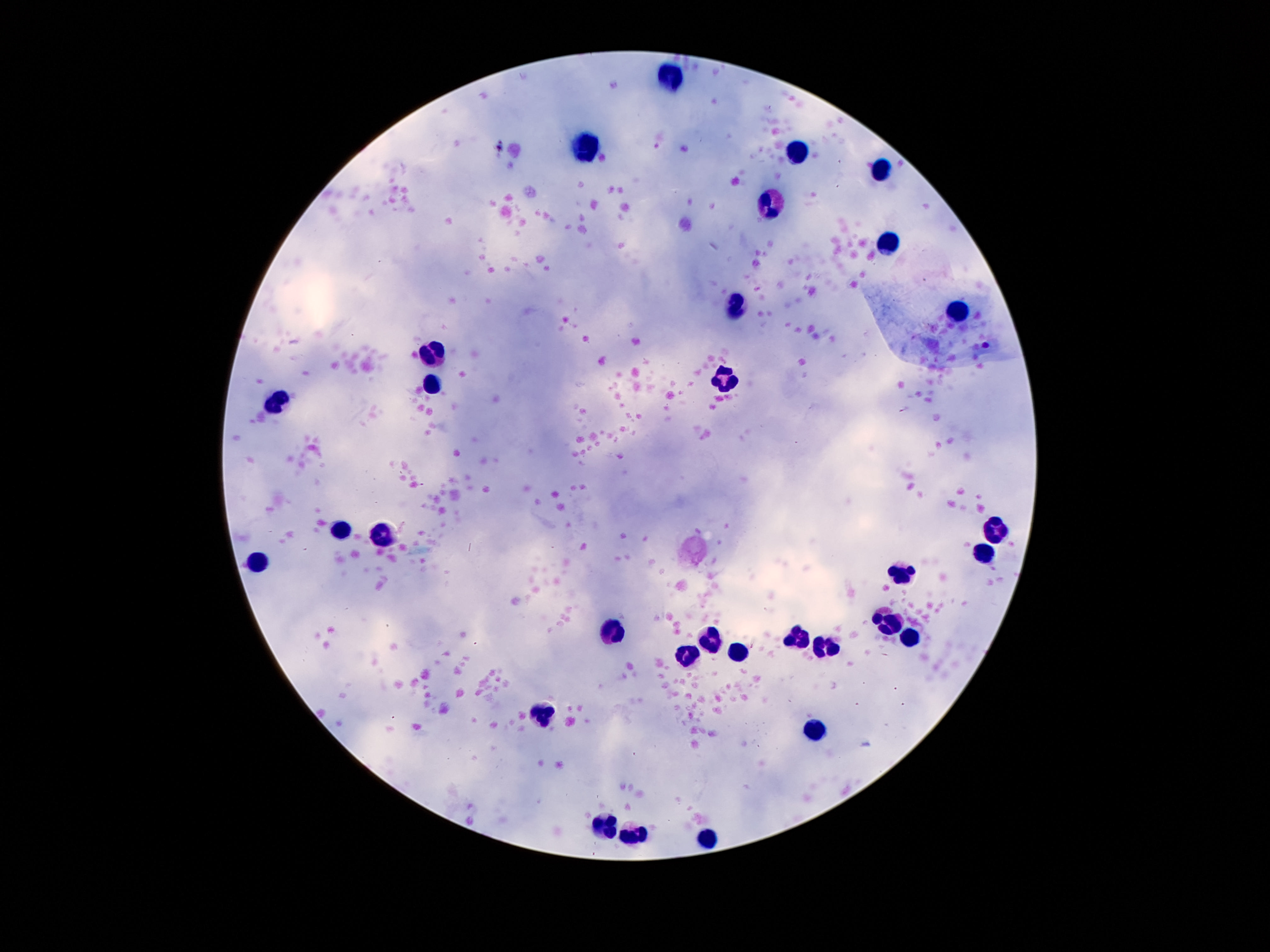

preparation = thick peripheral-blood smear
stain = Giemsa
patient malaria status = not infected
capture = smartphone camera through the microscope eyepiece
image size = 1270×952 pixels
leukocyte locations = approximate centers as {x, y} in pixels: {671, 75}, {586, 146}, {794, 152}, {880, 169}, {772, 204}, {892, 245}, {737, 305}, {957, 309}, {430, 355}, {724, 380}, {433, 384}, {279, 402}, {996, 529}, {338, 532}, {383, 536}, {979, 556}, {256, 566}, {898, 572}, {889, 624}, {607, 632}, {796, 637}, {712, 638}, {905, 639}, {825, 651}, {690, 653}, {738, 653}, {542, 714}, {813, 730}, {607, 826}, {634, 834}, {705, 837}
field of view = one from this slide
magnification = 100x